State the blood parasite species.
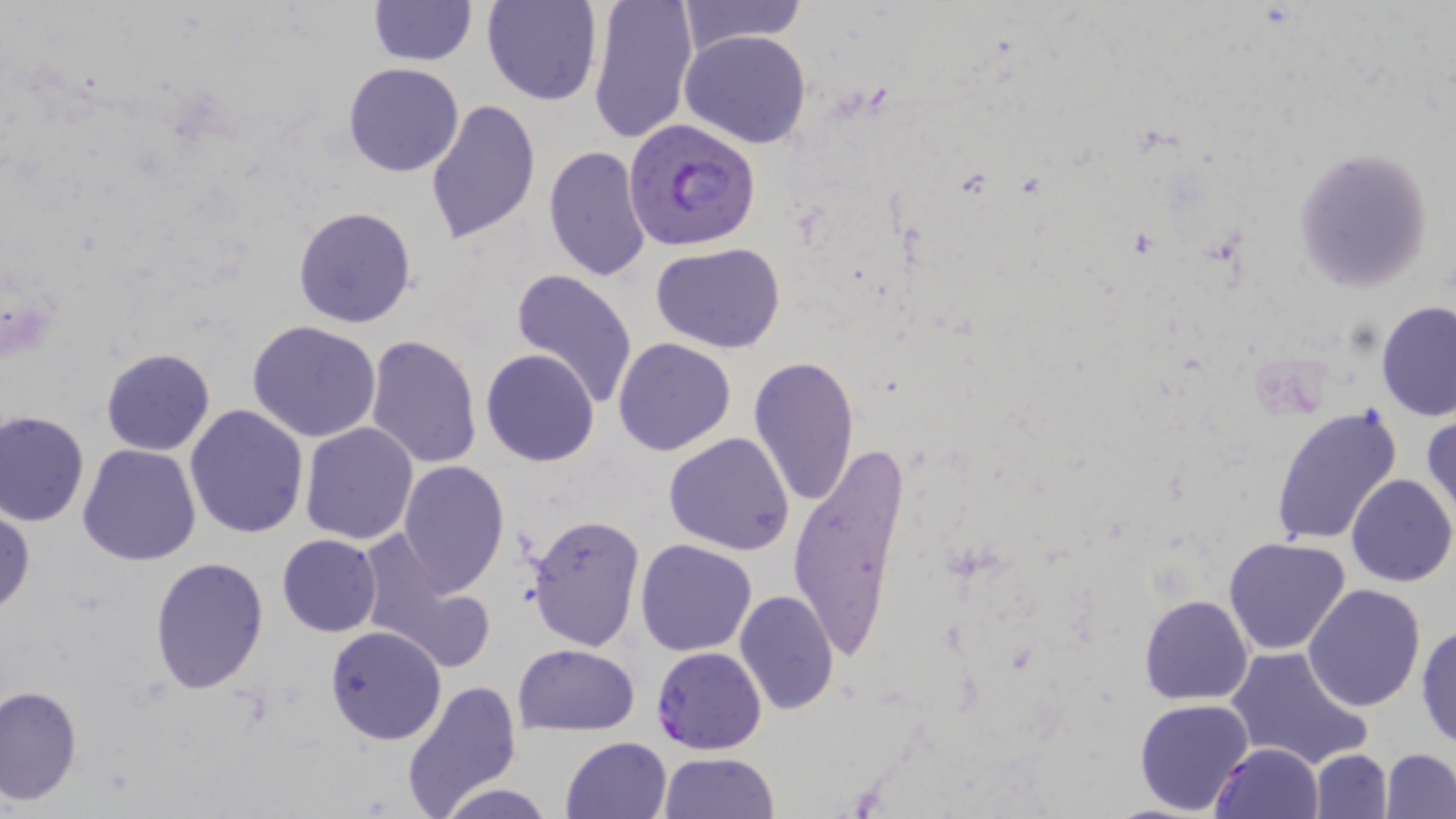
Plasmodium falciparum.

field_of_view: one of a larger specimen
plasmodium_falciparum_infected_red_blood_cell_locations: 'approximate bounding boxes as named x1/y1/x2/y2 corners in pixels: (x1=624, y1=117, x2=762, y2=251), (x1=651, y1=646, x2=767, y2=753)'
image_size: 1456×819 pixels
preparation: thin blood film
magnification: 1000x
uninfected_red_blood_cell_locations: 'approximate bounding boxes as named x1/y1/x2/y2 corners in pixels: (x1=369, y1=0, x2=475, y2=66), (x1=482, y1=0, x2=602, y2=107), (x1=588, y1=0, x2=697, y2=144), (x1=675, y1=0, x2=807, y2=55), (x1=681, y1=28, x2=813, y2=148), (x1=342, y1=61, x2=465, y2=177), (x1=424, y1=98, x2=542, y2=244), (x1=1293, y1=144, x2=1435, y2=291), (x1=542, y1=145, x2=652, y2=285), (x1=293, y1=205, x2=418, y2=329), (x1=651, y1=242, x2=785, y2=351), (x1=509, y1=269, x2=638, y2=409), (x1=1374, y1=301, x2=1456, y2=422), (x1=248, y1=321, x2=382, y2=442), (x1=366, y1=334, x2=483, y2=470), (x1=613, y1=337, x2=738, y2=456), (x1=100, y1=347, x2=215, y2=456), (x1=481, y1=348, x2=600, y2=467), (x1=748, y1=354, x2=861, y2=509), (x1=184, y1=404, x2=309, y2=539), (x1=1270, y1=406, x2=1404, y2=547), (x1=1, y1=409, x2=90, y2=527), (x1=1423, y1=411, x2=1455, y2=526), (x1=299, y1=422, x2=419, y2=545), (x1=663, y1=432, x2=796, y2=555), (x1=785, y1=438, x2=915, y2=667), (x1=78, y1=444, x2=202, y2=566), (x1=396, y1=458, x2=510, y2=597), (x1=1347, y1=472, x2=1456, y2=588), (x1=0, y1=506, x2=34, y2=618), (x1=525, y1=513, x2=646, y2=652), (x1=277, y1=534, x2=382, y2=637), (x1=357, y1=536, x2=496, y2=673), (x1=1223, y1=536, x2=1351, y2=656), (x1=635, y1=538, x2=758, y2=656), (x1=149, y1=555, x2=269, y2=694), (x1=1303, y1=583, x2=1427, y2=712), (x1=733, y1=588, x2=841, y2=716), (x1=1139, y1=594, x2=1254, y2=705), (x1=1415, y1=623, x2=1456, y2=749), (x1=325, y1=625, x2=447, y2=745), (x1=512, y1=644, x2=639, y2=734), (x1=1225, y1=645, x2=1373, y2=771), (x1=401, y1=681, x2=522, y2=818), (x1=0, y1=684, x2=82, y2=806), (x1=1134, y1=698, x2=1255, y2=816), (x1=560, y1=736, x2=671, y2=819), (x1=1211, y1=742, x2=1324, y2=819), (x1=1380, y1=748, x2=1455, y2=817), (x1=1309, y1=749, x2=1392, y2=817), (x1=659, y1=751, x2=781, y2=818), (x1=435, y1=782, x2=556, y2=819)'
modality: optical microscopy
stain: May-Grünwald-Giemsa